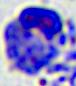

identification = leukocyte
modality = photomicrograph
magnification = 400x